Locate every blood parasite and identify its species.
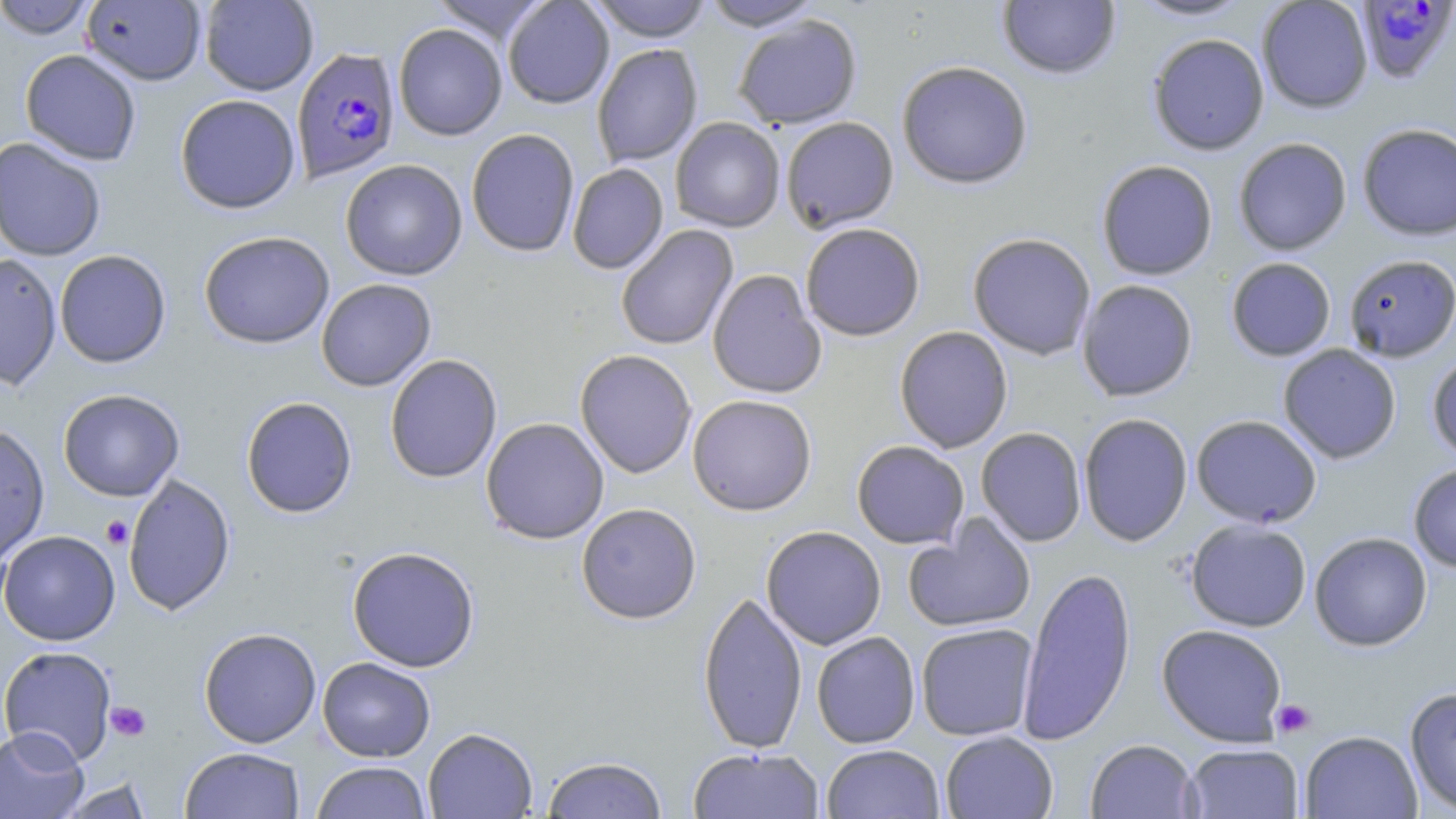
Approximate bounding boxes as named x1/y1/x2/y2 corners in pixels.
Plasmodium falciparum-infected red blood cells: (x1=1355, y1=1, x2=1455, y2=84), (x1=291, y1=46, x2=400, y2=183).
No Plasmodium ovale, Plasmodium malariae, Plasmodium vivax, Babesia divergens, or Trypanosoma brucei observed.

slide-level diagnosis = Plasmodium falciparum
magnification = 1000x
image size = 1456×819 pixels
uninfected red blood cell locations = approximate bounding boxes as named x1/y1/x2/y2 corners in pixels: (x1=0, y1=0, x2=98, y2=40), (x1=81, y1=0, x2=207, y2=86), (x1=199, y1=0, x2=318, y2=95), (x1=430, y1=0, x2=551, y2=45), (x1=503, y1=0, x2=614, y2=109), (x1=588, y1=0, x2=714, y2=42), (x1=997, y1=0, x2=1121, y2=79), (x1=1130, y1=0, x2=1251, y2=21), (x1=1256, y1=0, x2=1373, y2=113), (x1=700, y1=1, x2=825, y2=31), (x1=733, y1=15, x2=862, y2=129), (x1=393, y1=23, x2=507, y2=141), (x1=1147, y1=33, x2=1270, y2=155), (x1=591, y1=43, x2=703, y2=168), (x1=20, y1=49, x2=142, y2=165), (x1=896, y1=60, x2=1033, y2=189), (x1=175, y1=94, x2=301, y2=214), (x1=780, y1=116, x2=899, y2=233), (x1=670, y1=117, x2=786, y2=232), (x1=1357, y1=123, x2=1456, y2=240), (x1=466, y1=128, x2=580, y2=257), (x1=0, y1=137, x2=107, y2=261), (x1=1233, y1=137, x2=1352, y2=256), (x1=339, y1=159, x2=468, y2=280), (x1=1096, y1=159, x2=1218, y2=280), (x1=567, y1=163, x2=669, y2=274), (x1=800, y1=222, x2=926, y2=341), (x1=615, y1=225, x2=739, y2=350), (x1=198, y1=230, x2=335, y2=349), (x1=967, y1=233, x2=1096, y2=360), (x1=54, y1=249, x2=171, y2=368), (x1=0, y1=252, x2=63, y2=392), (x1=1342, y1=254, x2=1456, y2=362), (x1=1225, y1=257, x2=1336, y2=361), (x1=707, y1=269, x2=827, y2=399), (x1=316, y1=278, x2=436, y2=392), (x1=1076, y1=279, x2=1198, y2=402), (x1=894, y1=326, x2=1013, y2=453), (x1=1278, y1=344, x2=1402, y2=464), (x1=574, y1=349, x2=697, y2=478), (x1=1427, y1=351, x2=1456, y2=463), (x1=384, y1=354, x2=503, y2=484), (x1=57, y1=388, x2=185, y2=502), (x1=687, y1=394, x2=817, y2=516), (x1=241, y1=396, x2=357, y2=518), (x1=1078, y1=412, x2=1193, y2=546), (x1=1191, y1=414, x2=1322, y2=528), (x1=480, y1=417, x2=609, y2=544), (x1=0, y1=423, x2=50, y2=564), (x1=975, y1=427, x2=1087, y2=547), (x1=851, y1=440, x2=969, y2=549), (x1=1408, y1=462, x2=1456, y2=572), (x1=122, y1=474, x2=236, y2=616), (x1=576, y1=502, x2=702, y2=624), (x1=903, y1=514, x2=1037, y2=634), (x1=1185, y1=518, x2=1312, y2=632), (x1=761, y1=525, x2=887, y2=650), (x1=0, y1=530, x2=120, y2=646), (x1=1309, y1=531, x2=1432, y2=651), (x1=346, y1=546, x2=481, y2=672), (x1=1016, y1=564, x2=1137, y2=745), (x1=697, y1=591, x2=808, y2=754), (x1=915, y1=623, x2=1038, y2=741), (x1=1156, y1=623, x2=1288, y2=746), (x1=198, y1=627, x2=322, y2=747), (x1=811, y1=631, x2=921, y2=748), (x1=0, y1=645, x2=117, y2=764), (x1=317, y1=657, x2=436, y2=762), (x1=1404, y1=686, x2=1456, y2=815), (x1=0, y1=726, x2=89, y2=819), (x1=422, y1=727, x2=538, y2=818), (x1=940, y1=730, x2=1058, y2=819), (x1=1300, y1=730, x2=1422, y2=819), (x1=1085, y1=739, x2=1199, y2=819), (x1=1183, y1=743, x2=1304, y2=818), (x1=821, y1=744, x2=945, y2=818), (x1=179, y1=746, x2=305, y2=819), (x1=687, y1=747, x2=825, y2=819), (x1=542, y1=755, x2=668, y2=818), (x1=310, y1=761, x2=432, y2=819), (x1=54, y1=778, x2=154, y2=818)
modality = optical microscopy
preparation = thin blood smear
platelet locations = approximate bounding boxes as named x1/y1/x2/y2 corners in pixels: (x1=101, y1=515, x2=133, y2=549), (x1=1271, y1=699, x2=1316, y2=738), (x1=105, y1=701, x2=151, y2=742)
stain = May-Grünwald-Giemsa
field of view = one of a larger specimen